State which parasite is depicted.
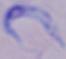
A trypanosome.

modality = photomicrograph
magnification = 1000x